Locate every leukocyte (white blood cell).
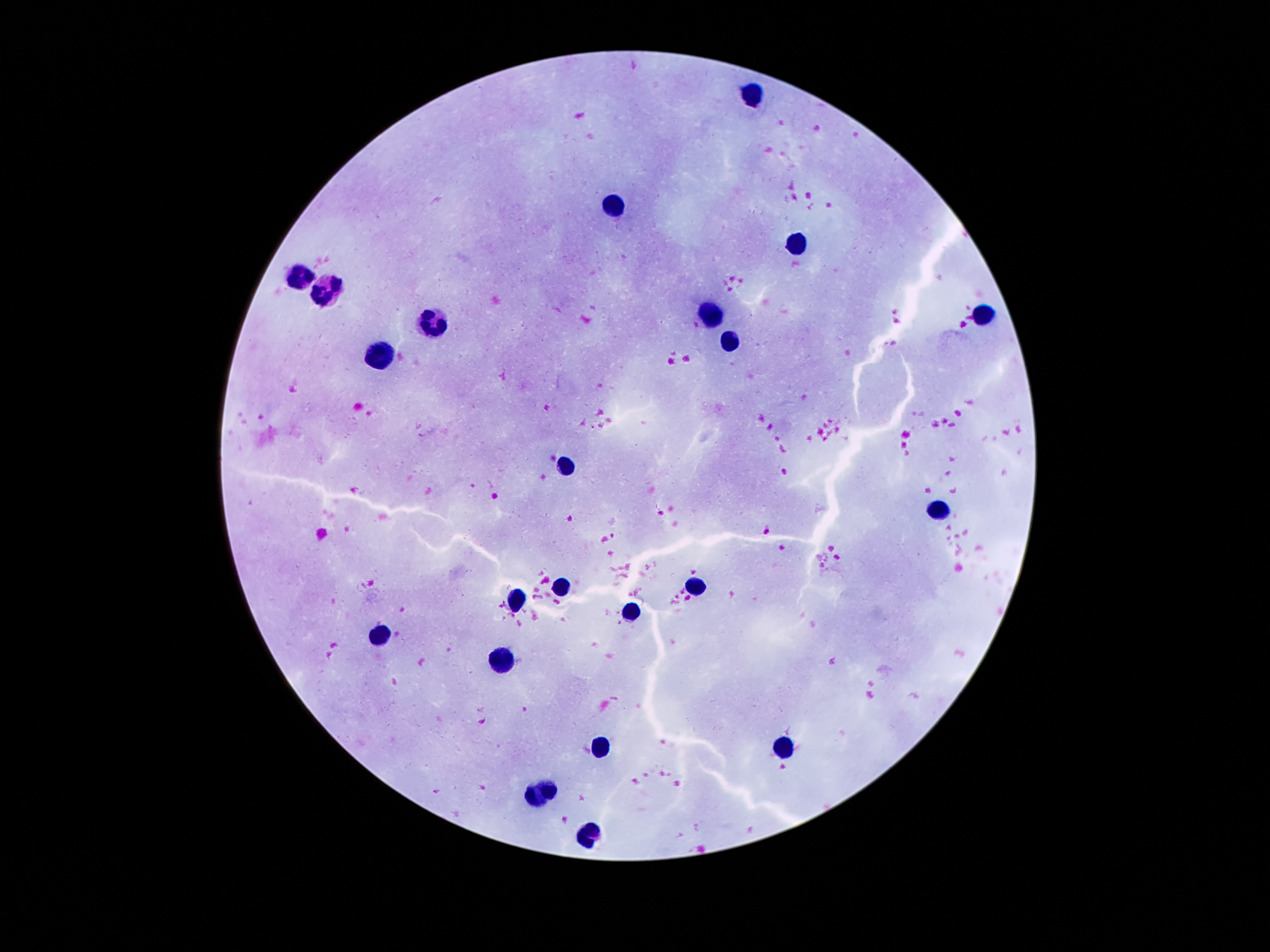
Approximate object centers, in pixels from the top-left corner.
Leukocytes: (x=752, y=93), (x=613, y=204), (x=795, y=242), (x=298, y=273), (x=328, y=288), (x=983, y=314), (x=711, y=316), (x=437, y=323), (x=731, y=341), (x=375, y=356), (x=562, y=468), (x=938, y=510), (x=695, y=585), (x=561, y=587), (x=514, y=601), (x=630, y=612), (x=382, y=635), (x=502, y=662), (x=600, y=747), (x=782, y=748), (x=543, y=796), (x=584, y=834).

Photographed through the microscope eyepiece with a smartphone camera. Patient malaria status: uninfected. Thick peripheral-blood smear. Giemsa stain. Image is 1270×952 pixels. Single field of view. 100x magnification.